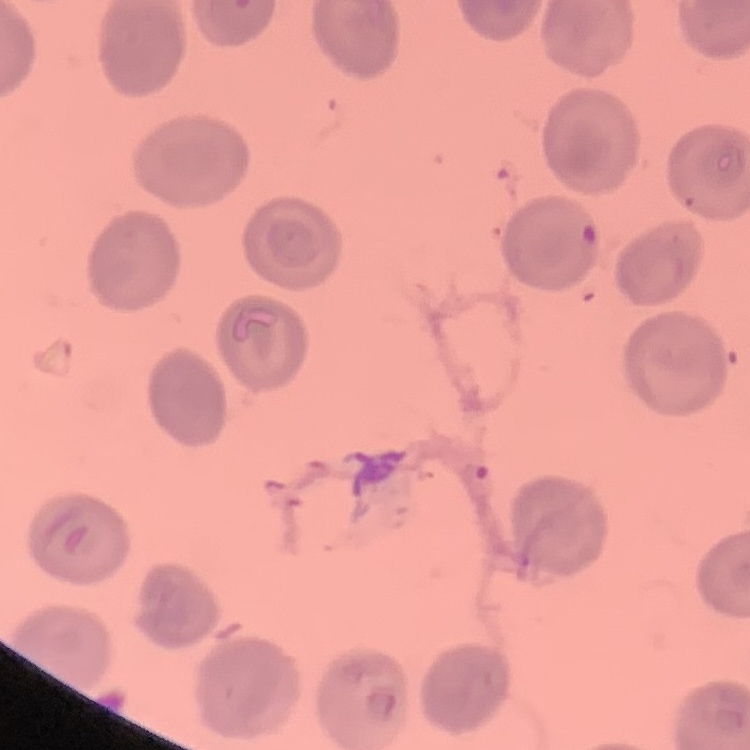
Summary:
  - Erythrocyte morphology: no rouleaux formation
  - Preparation: thin blood smear
  - Image type: one tile cut from a larger photomicrograph
  - Stain: Field's or Giemsa